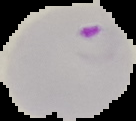 Result: malaria parasites detected. From a thin blood smear. Image is 136×121 pixels. Cell region segmented out of the field of view; the surrounding area is masked to black.